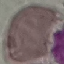
Result: negative for malaria parasites. Photographed with a smartphone camera at the microscope eyepiece. Automatically extracted cell patch, resized to 64 × 64 pixels. Thin blood film. Giemsa-stained preparation.